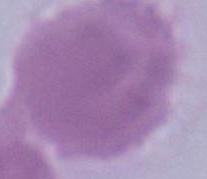

{
  "magnification": "1000x",
  "identification": "erythrocyte",
  "modality": "photomicrograph"
}